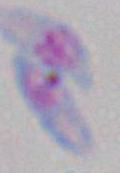
Summary:
  - Magnification: 1000x
  - Identification: Toxoplasma gondii
  - Modality: photomicrograph